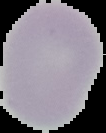
Cell region segmented out of the field of view; the surrounding area is masked to black. Result: negative for Plasmodium parasites. Image is 106×133 pixels. From a thin blood film.